Assess this cell for malaria.
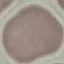
It is uninfected.

Thin blood film. Cell patch, automatically extracted from a larger field of view and resized to 64 × 64 pixels. Giemsa-stained preparation. Photographed with a smartphone camera at the microscope eyepiece.